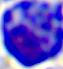 Captured at 400x magnification. Micrograph. A white blood cell is seen.